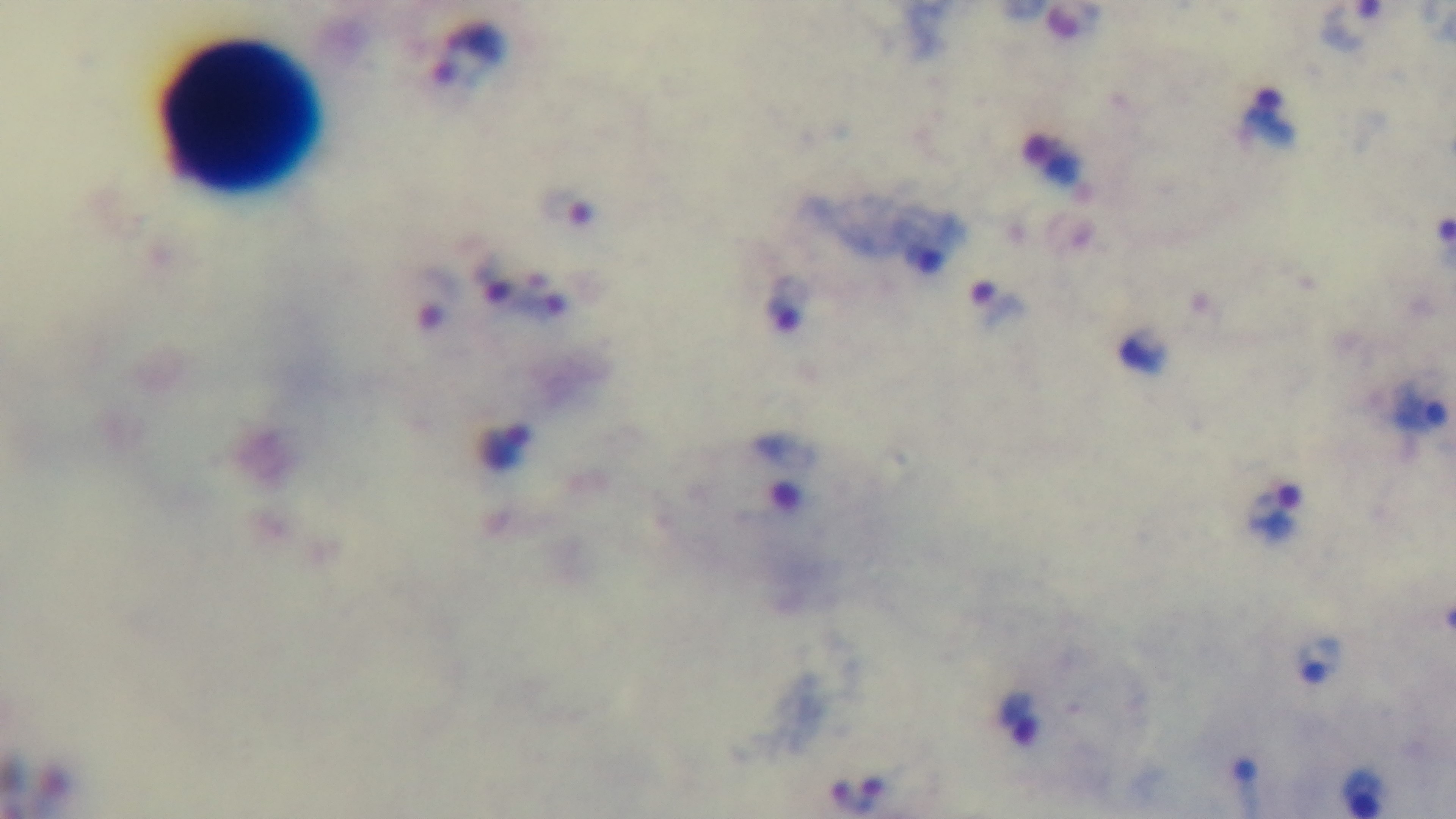
field of view = one from the slide
objective = 100x oil immersion
capture = mounted 4K digital camera
malaria status = positive
modality = light microscopy
preparation = thick blood film
stain = Giemsa